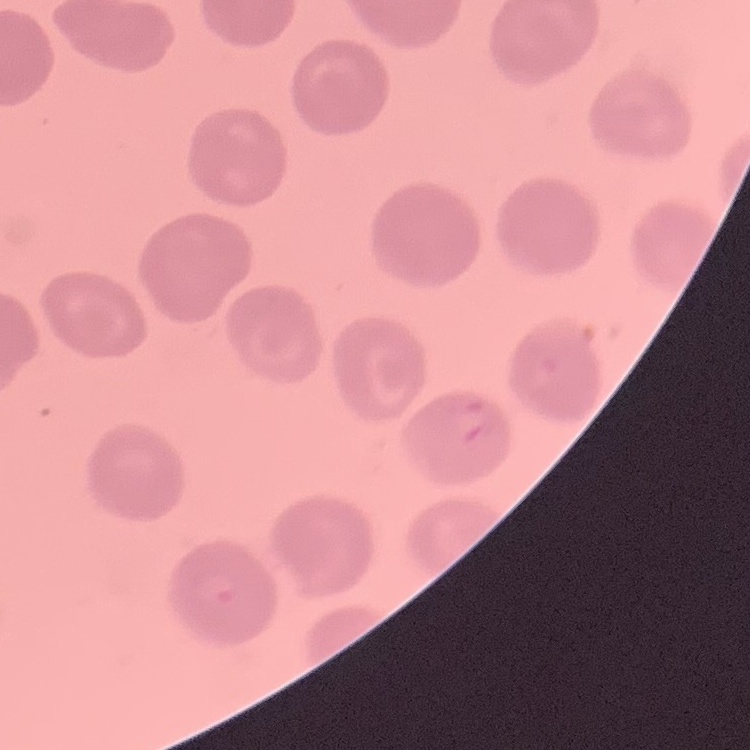

erythrocyte_morphology: no rouleaux formation
image_type: square crop of a larger photomicrograph
stain: Field's or Giemsa
preparation: thin blood film